Give the position of every malaria parasite.
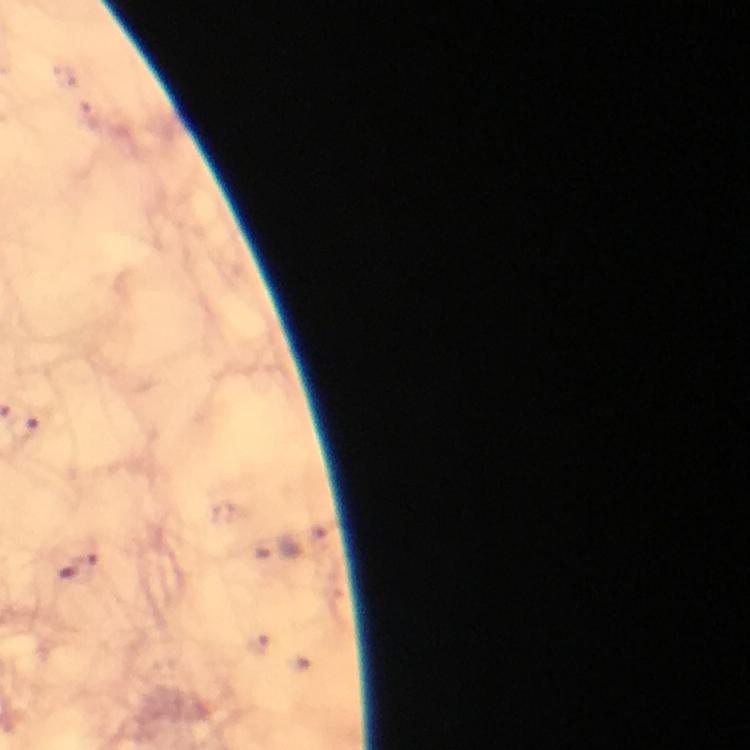

Approximate centers as (x, y) in pixels.
Malaria parasites: (88, 564), (68, 572).

Summary:
  - Preparation: thick smear
  - Magnification: 100x
  - Immersion oil: used
  - Cropped from: a single field of view
  - Image size: 750×750 pixels
  - Capture: smartphone mounted on the microscope
  - Context: from a diagnostic examination for malaria
  - Stain: Giemsa